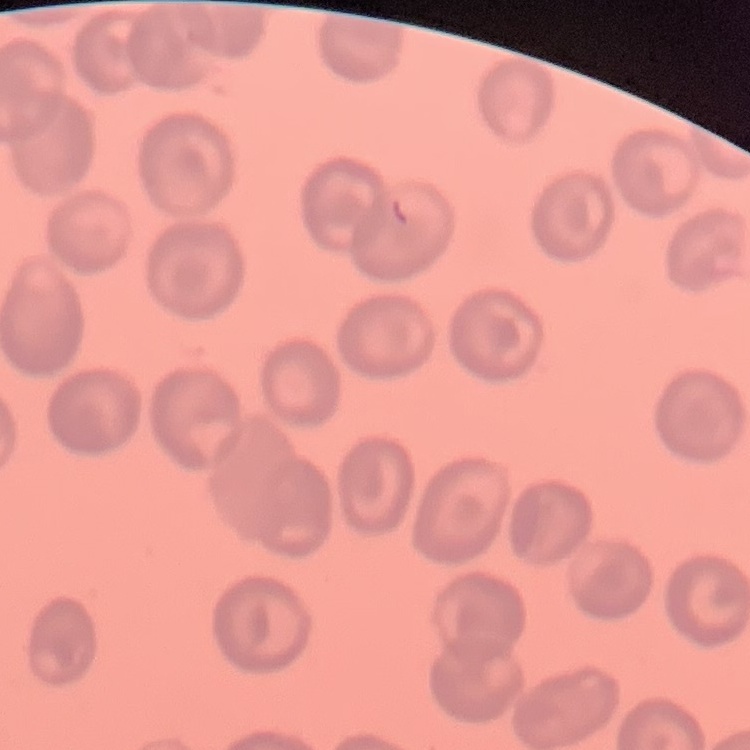

red blood cell morphology = no rouleaux formation
image type = one tile cut from a larger photomicrograph
preparation = thin peripheral smear
stain = Field's or Giemsa